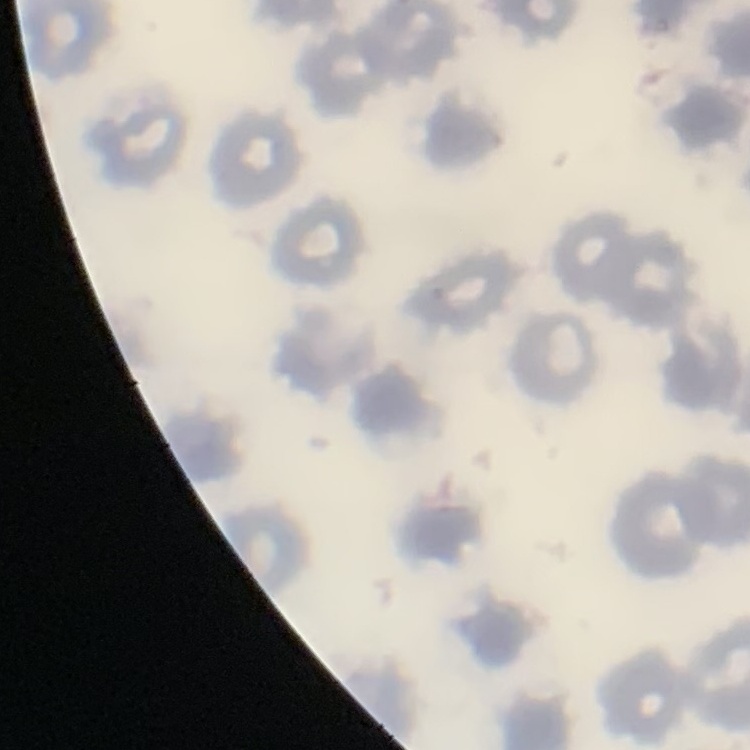

erythrocyte morphology = no rouleaux formation
stain = Field's or Giemsa
image type = square crop of a larger photomicrograph
preparation = thin peripheral smear